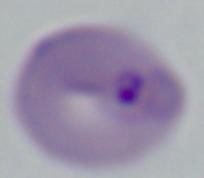

A Babesia parasite is seen. 1000x magnification. Micrograph.